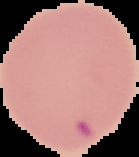
Summary:
  - Image type: segmented cell region with the area outside set to black
  - Malaria status: parasitized
  - Preparation: thin blood smear
  - Image size: 139×157 pixels